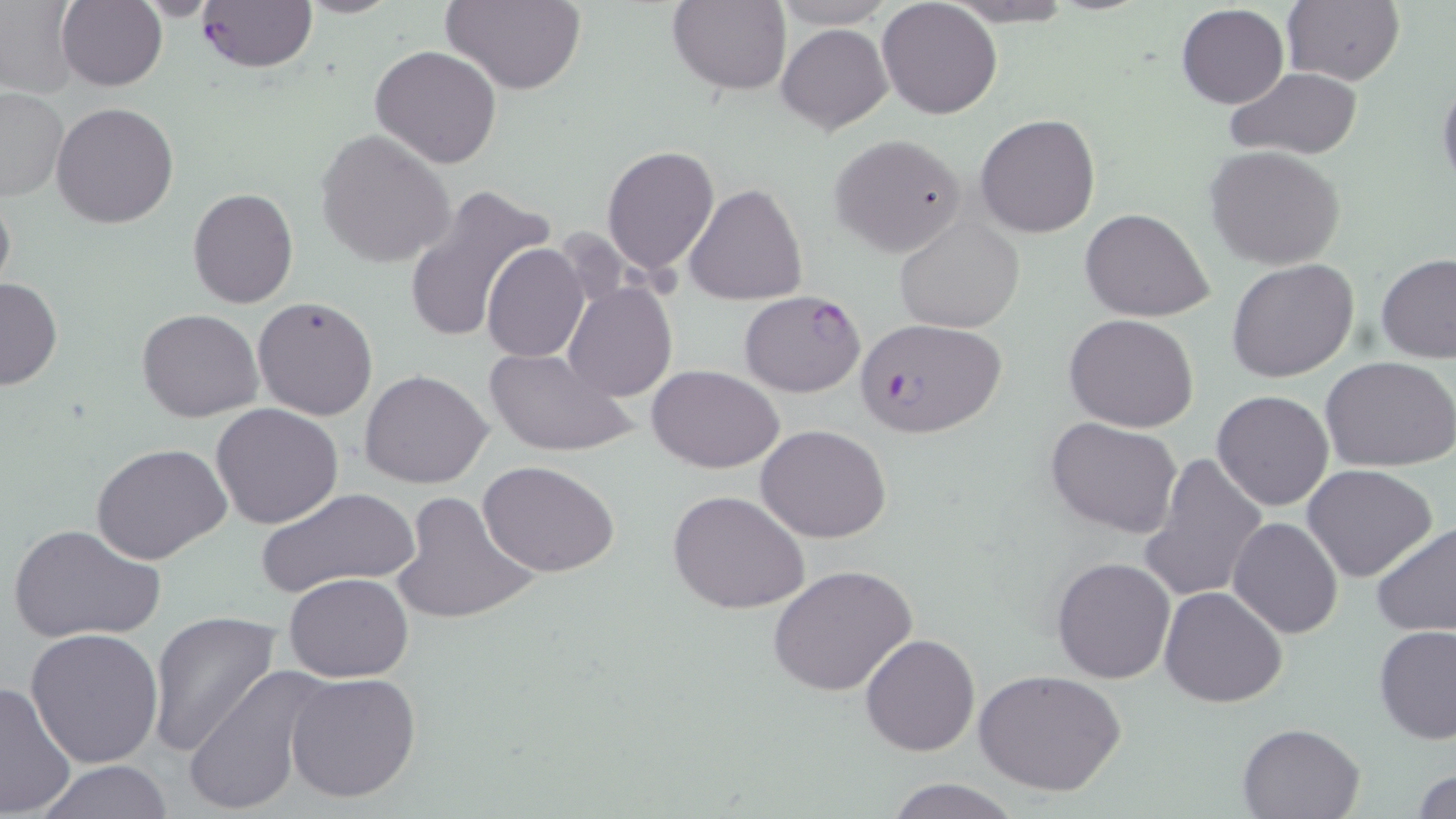

Summary:
  - Coordinate format: approximate bounding boxes as (x1, y1, x2, y2) in pixels
  - Plasmodium falciparum-infected red blood cell locations: (197, 1, 317, 72), (740, 289, 867, 398), (855, 319, 1010, 438)
  - Uninfected red blood cell locations: (58, 0, 167, 90), (441, 0, 587, 94), (667, 0, 792, 95), (771, 0, 896, 27), (1281, 0, 1403, 87), (877, 1, 1003, 119), (938, 2, 1083, 27), (1, 3, 80, 98), (1176, 4, 1289, 110), (776, 23, 891, 134), (371, 44, 503, 169), (1226, 67, 1362, 160), (1437, 73, 1456, 195), (1, 86, 66, 201), (51, 101, 179, 229), (975, 113, 1102, 240), (315, 128, 456, 268), (830, 133, 965, 256), (1204, 145, 1346, 269), (602, 146, 719, 276), (0, 183, 16, 305), (684, 183, 808, 307), (401, 184, 552, 342), (187, 187, 298, 309), (1079, 207, 1213, 321), (895, 215, 1024, 332), (482, 243, 590, 365), (1377, 253, 1456, 364), (1226, 259, 1360, 383), (0, 275, 63, 390), (563, 282, 677, 402), (252, 296, 379, 422), (137, 309, 264, 424), (1064, 313, 1199, 433), (486, 346, 637, 457), (1323, 356, 1456, 473), (649, 364, 785, 473), (359, 370, 494, 490), (1211, 390, 1335, 511), (210, 404, 343, 530), (1046, 416, 1184, 537), (756, 424, 891, 544), (92, 443, 230, 567), (1138, 452, 1269, 604), (478, 460, 621, 577), (1302, 464, 1438, 581), (257, 488, 418, 601), (668, 488, 811, 614), (391, 490, 540, 626), (1228, 517, 1342, 638), (1370, 522, 1456, 637), (11, 525, 163, 645), (1051, 555, 1177, 684), (770, 565, 919, 698), (283, 572, 414, 682), (1159, 586, 1287, 708), (145, 610, 283, 757), (1375, 625, 1456, 744), (25, 627, 164, 768), (859, 633, 980, 757), (179, 668, 327, 816), (974, 669, 1127, 797), (285, 672, 422, 803), (0, 681, 76, 817), (1237, 720, 1366, 818), (31, 761, 177, 817), (1412, 767, 1456, 817), (885, 777, 1023, 818)
  - Slide-level diagnosis: Plasmodium falciparum
  - Image size: 1456×819 pixels
  - Field of view: one of a larger specimen
  - Magnification: 1000x
  - Preparation: thin blood film
  - Stain: May-Grünwald-Giemsa
  - Modality: light microscopy